State the preparation type.
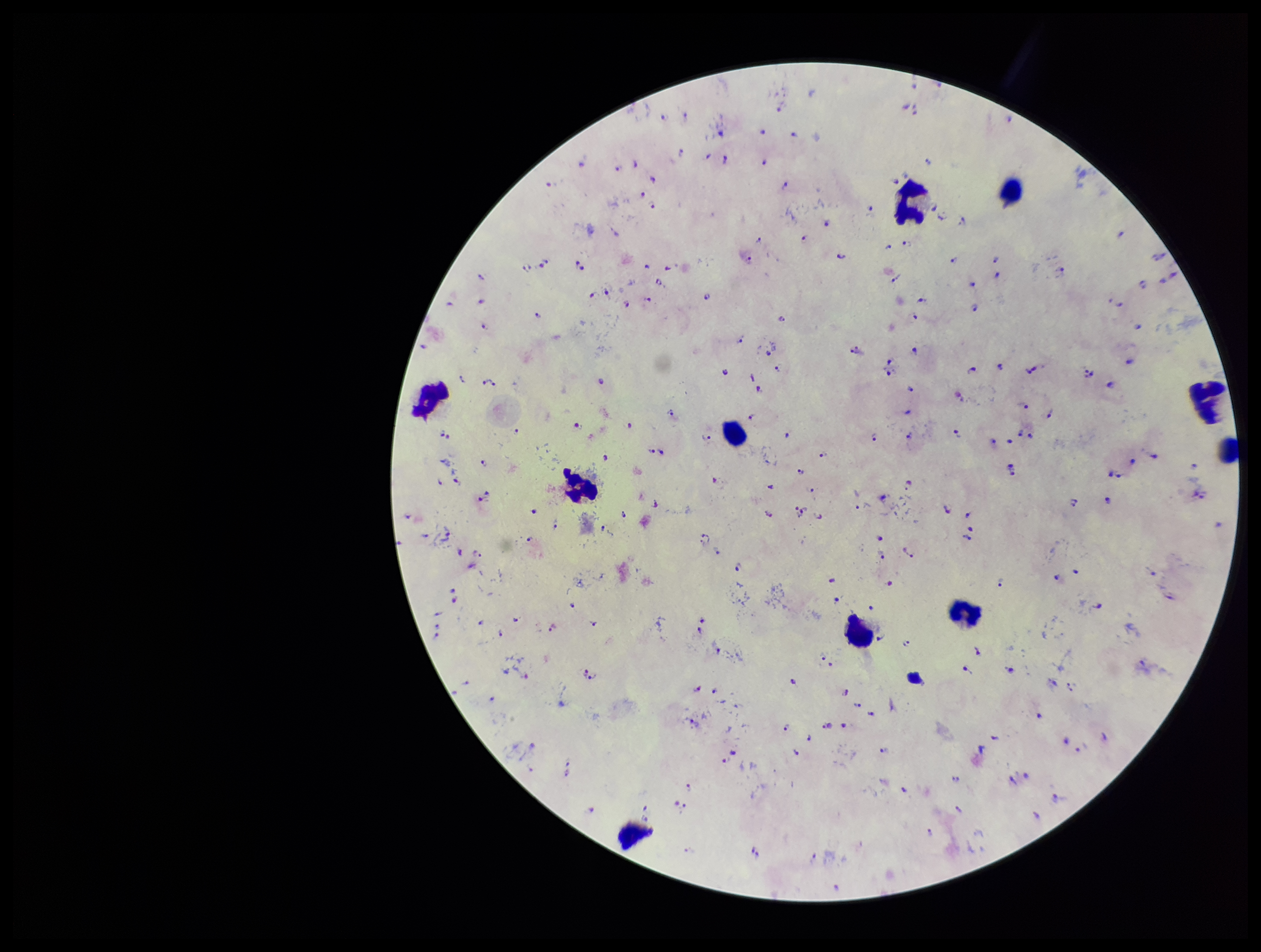

It is a thick blood smear.

stain = Giemsa
capture = smartphone photograph through the microscope eyepiece
field of view = one from this slide
patient malaria status = positive
species reported for this patient = Plasmodium falciparum
Plasmodium parasites = seen
parasite count = 180
leukocyte count = 10
image size = 1261×952 pixels